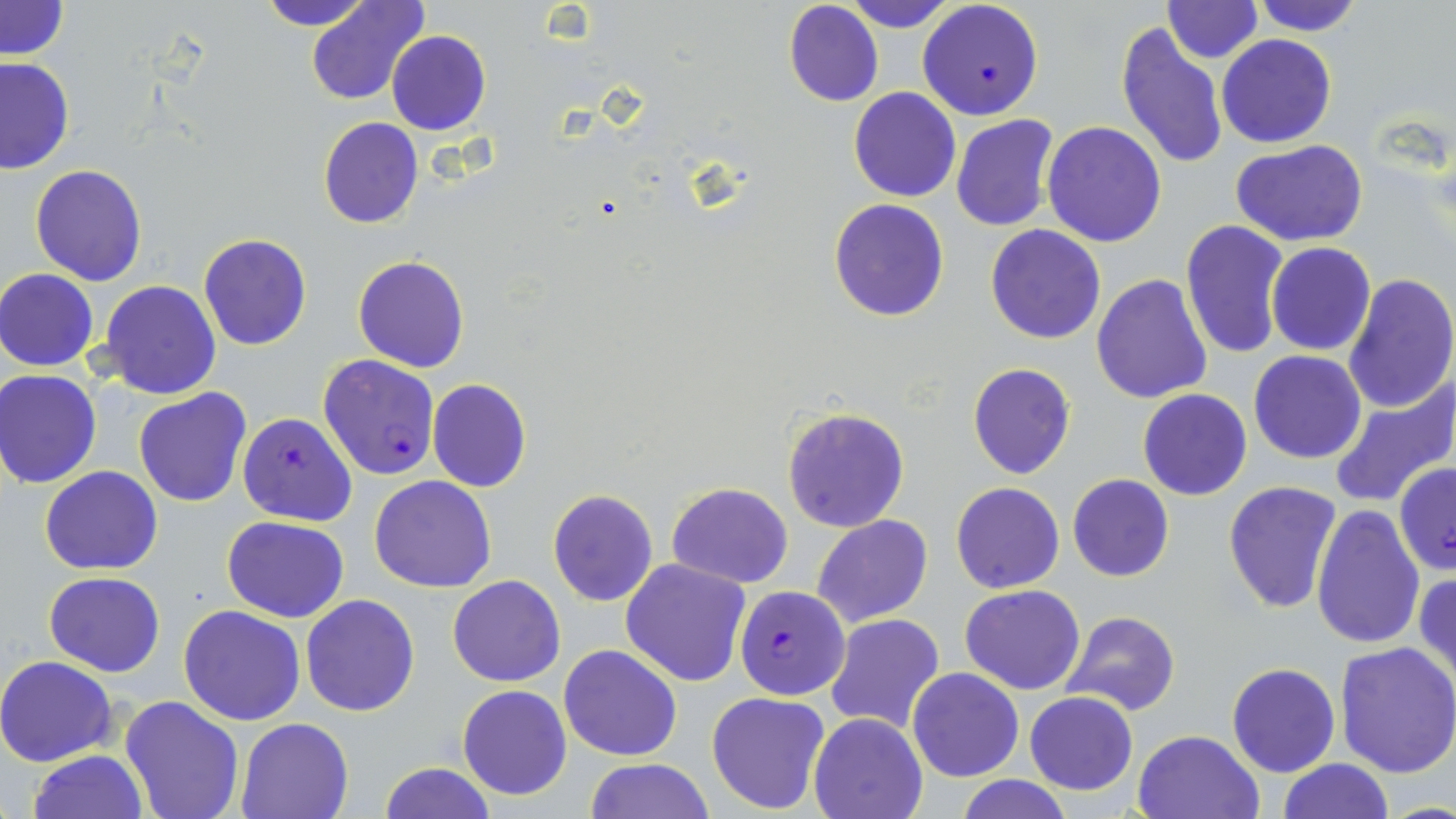
Approximate bounding boxes as (x1, y1, x2, y2) in pixels. Plasmodium falciparum-infected red blood cell locations: (917, 0, 1045, 121), (318, 354, 440, 480), (237, 412, 357, 526), (1393, 463, 1456, 577), (734, 585, 850, 700). Uninfected red blood cell locations: (254, 0, 375, 29), (307, 0, 430, 106), (1, 1, 70, 59), (782, 1, 884, 107), (843, 1, 956, 32), (1161, 1, 1263, 64), (1251, 1, 1365, 35), (1114, 22, 1230, 172), (386, 31, 492, 135), (1217, 34, 1336, 148), (0, 57, 74, 173), (849, 87, 961, 203), (951, 114, 1063, 234), (317, 117, 422, 229), (1040, 121, 1167, 248), (1231, 140, 1369, 246), (29, 165, 146, 285), (828, 200, 948, 321), (1179, 218, 1289, 361), (986, 225, 1107, 345), (198, 234, 312, 351), (1266, 242, 1375, 355), (352, 256, 470, 372), (1, 268, 99, 370), (1340, 272, 1455, 413), (1091, 274, 1213, 405), (98, 281, 222, 400), (1248, 350, 1367, 464), (967, 363, 1076, 480), (0, 368, 103, 488), (1328, 374, 1455, 509), (427, 378, 532, 492), (133, 388, 252, 508), (1137, 388, 1252, 501), (780, 407, 910, 532), (41, 466, 162, 575), (1067, 473, 1174, 582), (368, 475, 496, 592), (1221, 479, 1342, 614), (666, 481, 795, 588), (950, 481, 1065, 594), (547, 489, 660, 606), (1311, 504, 1426, 650), (812, 514, 934, 629), (222, 516, 350, 621), (620, 557, 752, 687), (1413, 571, 1456, 691), (44, 572, 165, 675), (447, 575, 566, 687), (960, 585, 1085, 695), (301, 593, 419, 716), (179, 604, 306, 725), (1062, 610, 1181, 716), (825, 613, 945, 734), (1334, 639, 1456, 779), (559, 643, 683, 761), (0, 655, 119, 767), (1227, 662, 1339, 777), (907, 667, 1025, 782), (456, 684, 573, 800), (706, 690, 832, 815), (1024, 691, 1137, 795), (119, 696, 245, 819), (807, 713, 927, 819), (237, 717, 353, 819), (1131, 729, 1263, 818), (27, 750, 147, 819), (582, 758, 717, 818), (1278, 758, 1392, 818), (379, 763, 496, 819), (955, 776, 1074, 818). Slide-level diagnosis: Plasmodium falciparum. Image is 1456×819 pixels. Thin blood smear. May-Grünwald-Giemsa-stained preparation. Captured at 1000x magnification. Optical microscopy. One field of a larger specimen.